Identify the parasite.
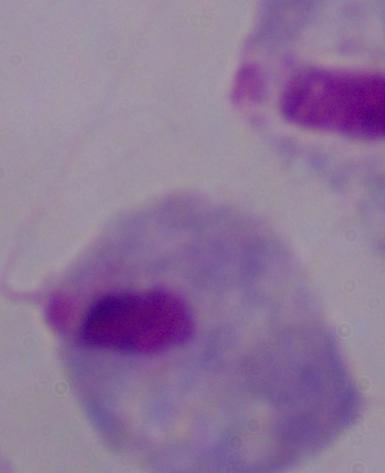

A trichomonad.

Summary:
  - Modality: photomicrograph
  - Magnification: 1000x